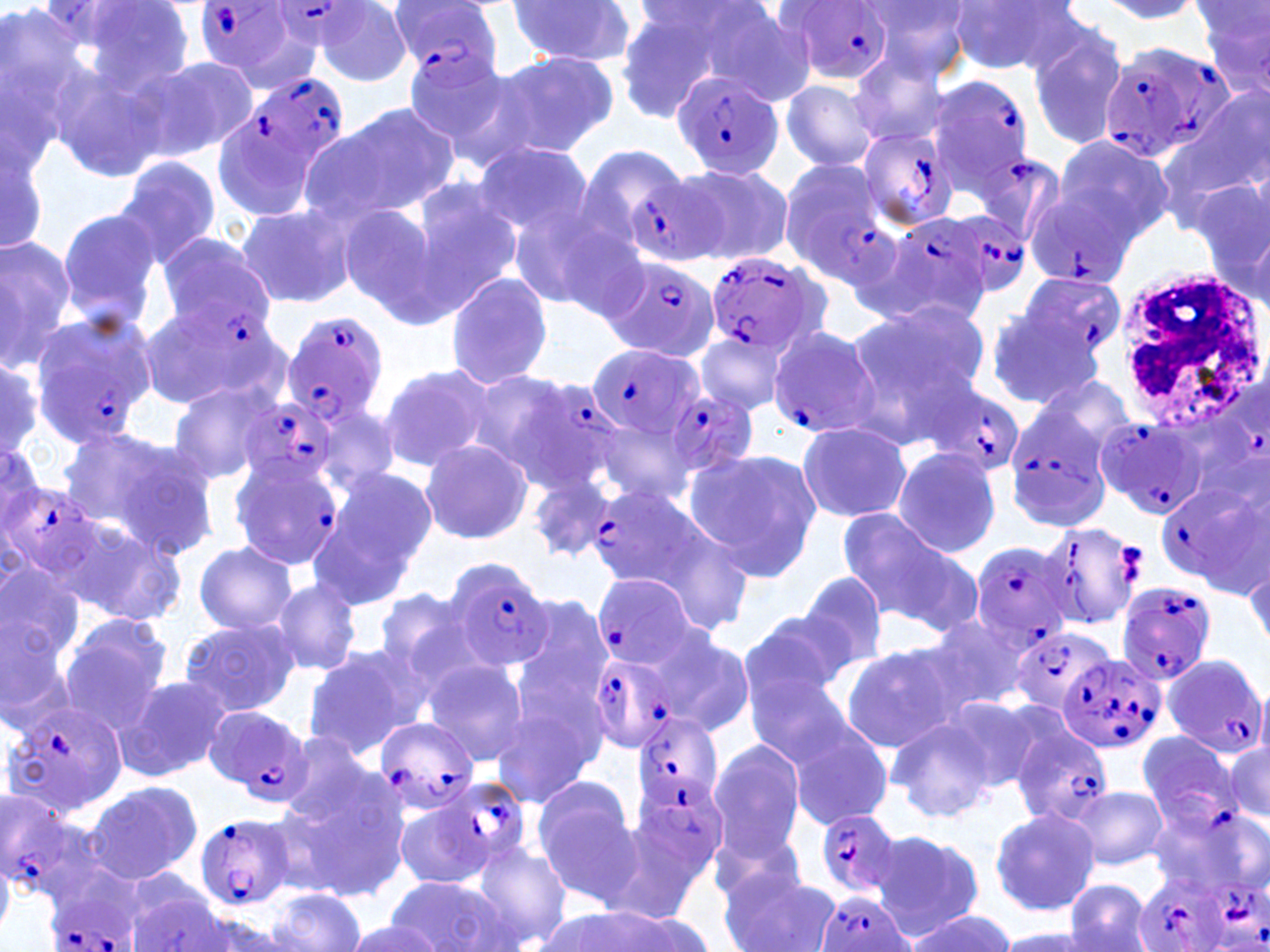 Approximate bounding boxes as (x1, y1, x2, y2) in pixels. Uninfected red blood cell locations: (38, 0, 198, 99), (507, 1, 639, 68), (861, 1, 973, 82), (948, 1, 1078, 74), (1098, 1, 1206, 23), (634, 2, 777, 62), (0, 3, 92, 162), (1197, 3, 1270, 99), (314, 4, 414, 86), (612, 4, 741, 121), (711, 5, 822, 105), (1026, 27, 1129, 151), (42, 36, 183, 184), (490, 49, 617, 158), (400, 51, 521, 158), (848, 53, 951, 145), (140, 54, 260, 162), (781, 79, 881, 172), (1160, 91, 1270, 228), (332, 101, 460, 215), (213, 110, 316, 223), (1054, 134, 1176, 244), (0, 138, 48, 257), (473, 142, 595, 246), (115, 156, 223, 267), (675, 162, 793, 265), (404, 178, 522, 309), (1193, 179, 1270, 295), (503, 194, 634, 318), (234, 204, 357, 308), (337, 204, 451, 324), (56, 208, 164, 333), (0, 234, 79, 366), (443, 271, 554, 392), (868, 299, 990, 401), (135, 301, 280, 414), (981, 306, 1102, 410), (840, 321, 977, 448), (697, 331, 787, 414), (0, 352, 44, 455), (376, 361, 494, 472), (1027, 374, 1140, 472), (165, 380, 279, 486), (310, 397, 402, 496), (587, 414, 699, 509), (795, 420, 910, 522), (60, 427, 216, 557), (419, 437, 534, 545), (891, 447, 1001, 556), (686, 450, 820, 584), (325, 466, 438, 578), (529, 473, 615, 561), (836, 508, 980, 638), (57, 514, 186, 627), (308, 521, 413, 612), (193, 540, 295, 636), (1246, 557, 1270, 653), (0, 558, 87, 664), (796, 570, 890, 673), (271, 578, 362, 676), (372, 587, 477, 686), (506, 595, 613, 740), (743, 607, 855, 706), (918, 614, 1033, 716), (0, 615, 81, 740), (57, 617, 170, 729), (179, 618, 300, 717), (644, 626, 756, 737), (841, 644, 963, 752), (302, 646, 424, 758), (421, 658, 529, 765), (744, 668, 858, 768), (114, 676, 230, 782), (488, 691, 605, 813), (944, 693, 1052, 793), (780, 713, 894, 832), (886, 715, 996, 825), (276, 730, 386, 829), (1187, 735, 1270, 834), (1226, 739, 1269, 824), (706, 742, 805, 862), (277, 777, 409, 903), (530, 778, 641, 905), (82, 780, 202, 886), (1069, 785, 1168, 870), (393, 797, 490, 891), (1148, 805, 1259, 892), (988, 808, 1099, 918), (707, 830, 813, 918), (871, 830, 984, 938), (469, 840, 573, 949), (719, 865, 840, 952), (386, 875, 511, 952), (1065, 878, 1153, 952), (125, 886, 233, 951), (266, 887, 367, 952), (556, 905, 702, 952), (176, 909, 292, 951), (910, 912, 1014, 952), (340, 917, 446, 952), (992, 929, 1094, 951). White blood cell locations: (1111, 262, 1266, 426). Plasmodium falciparum-infected red blood cell locations: (389, 0, 505, 78), (191, 1, 304, 81), (782, 1, 895, 85), (268, 2, 374, 55), (1099, 41, 1228, 164), (245, 70, 349, 175), (671, 70, 783, 178), (924, 76, 1035, 190), (855, 126, 961, 232), (971, 153, 1063, 248), (778, 156, 892, 280), (629, 181, 726, 260), (1022, 187, 1139, 290), (944, 208, 1038, 297), (857, 219, 987, 330), (152, 230, 272, 356), (703, 251, 825, 358), (602, 255, 720, 362), (1013, 273, 1120, 370), (280, 311, 388, 428), (25, 316, 156, 449), (765, 323, 880, 439), (588, 343, 702, 441), (470, 371, 612, 493), (926, 381, 1025, 480), (664, 388, 757, 478), (240, 396, 340, 494), (1007, 406, 1110, 529), (1095, 415, 1207, 520), (227, 456, 341, 570), (1155, 478, 1264, 589), (1, 481, 107, 580), (586, 484, 709, 593), (1043, 521, 1142, 629), (970, 541, 1075, 650), (443, 555, 556, 673), (589, 570, 705, 670), (1115, 580, 1217, 685), (1010, 623, 1117, 714), (588, 652, 679, 753), (1056, 654, 1165, 754), (1161, 654, 1269, 759), (5, 698, 128, 815), (206, 708, 313, 806), (631, 712, 722, 811), (374, 717, 478, 812), (1009, 724, 1114, 828), (1139, 730, 1244, 834), (435, 775, 533, 874), (637, 778, 726, 873), (0, 789, 98, 902), (817, 809, 906, 897), (190, 814, 298, 909), (1134, 871, 1230, 952), (41, 875, 143, 952), (1193, 879, 1270, 952), (816, 890, 914, 952). Slide-level diagnosis: Plasmodium falciparum. Thin blood smear. Captured at 1000x magnification. Single field of view. Optical microscopy. May-Grünwald-Giemsa-stained preparation. Image is 1270×952 pixels.